Comment on the morphology of the erythrocytes.
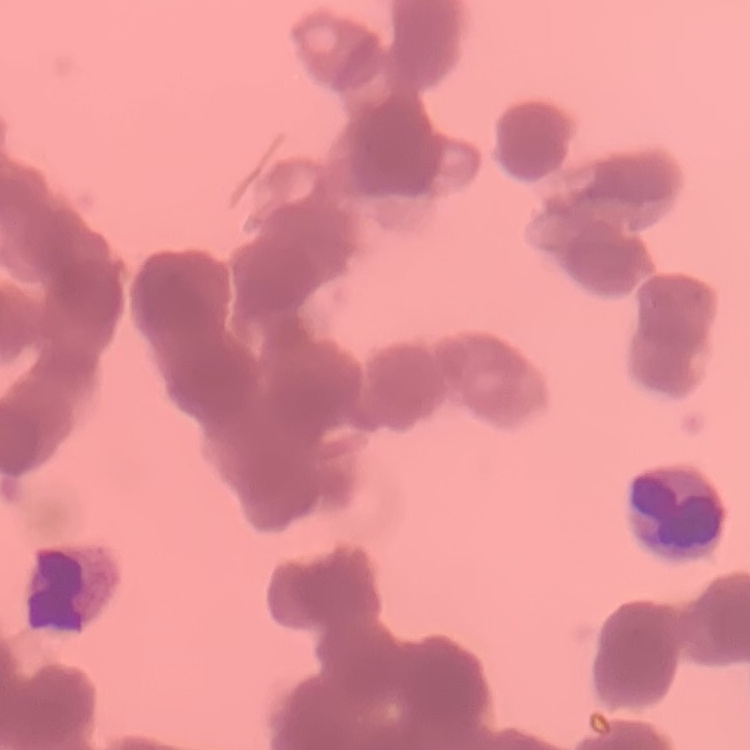

Rouleaux formation.

{
  "image_type": "one tile cut from a larger photomicrograph",
  "preparation": "thin blood smear",
  "stain": "Field's or Giemsa"
}